Locate every Plasmodium parasite.
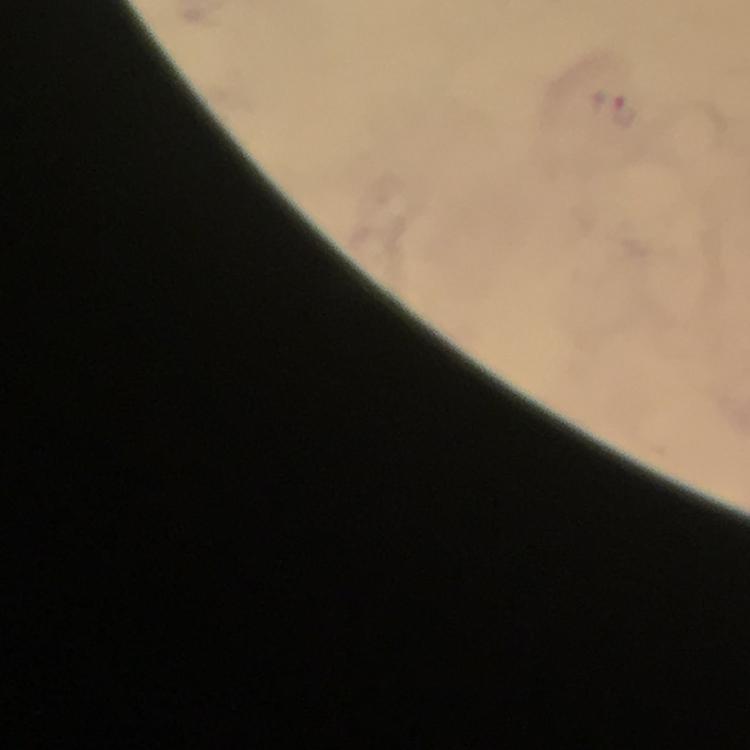
Approximate centers as (x, y) in pixels.
Plasmodium parasites: (623, 109).

{
  "cropped_from": "one field of view",
  "preparation": "thick smear",
  "context": "from a malaria diagnostic workup",
  "capture": "smartphone photograph through a microscope",
  "magnification": "100x",
  "immersion_oil": "applied",
  "stain": "Giemsa",
  "image_size": "750×750 pixels"
}